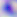
Summary:
  - Modality: micrograph
  - Identification: Toxoplasma gondii
  - Magnification: 400x